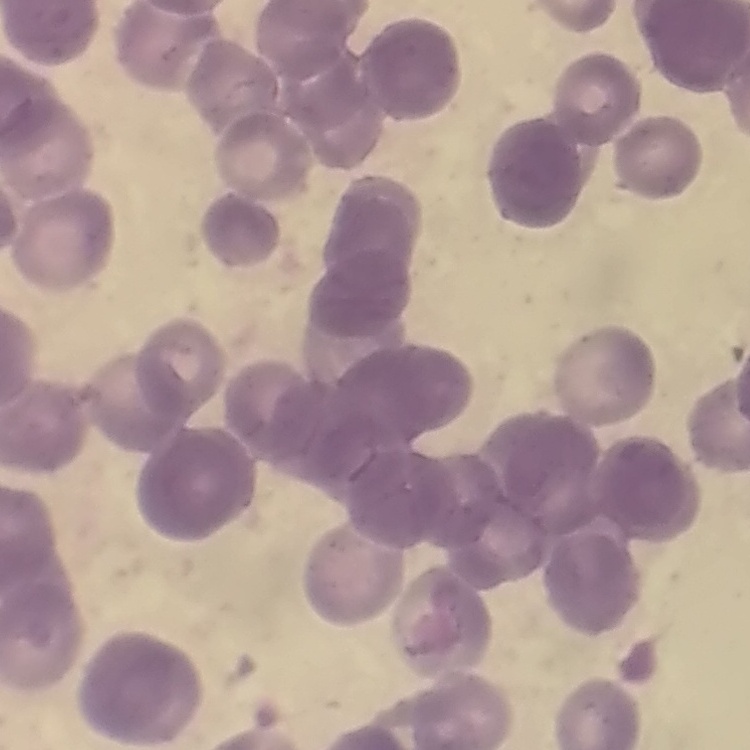

The erythrocytes exhibit rouleaux formation. Field's or Giemsa stain. Thin blood smear. Square crop of a larger photomicrograph.